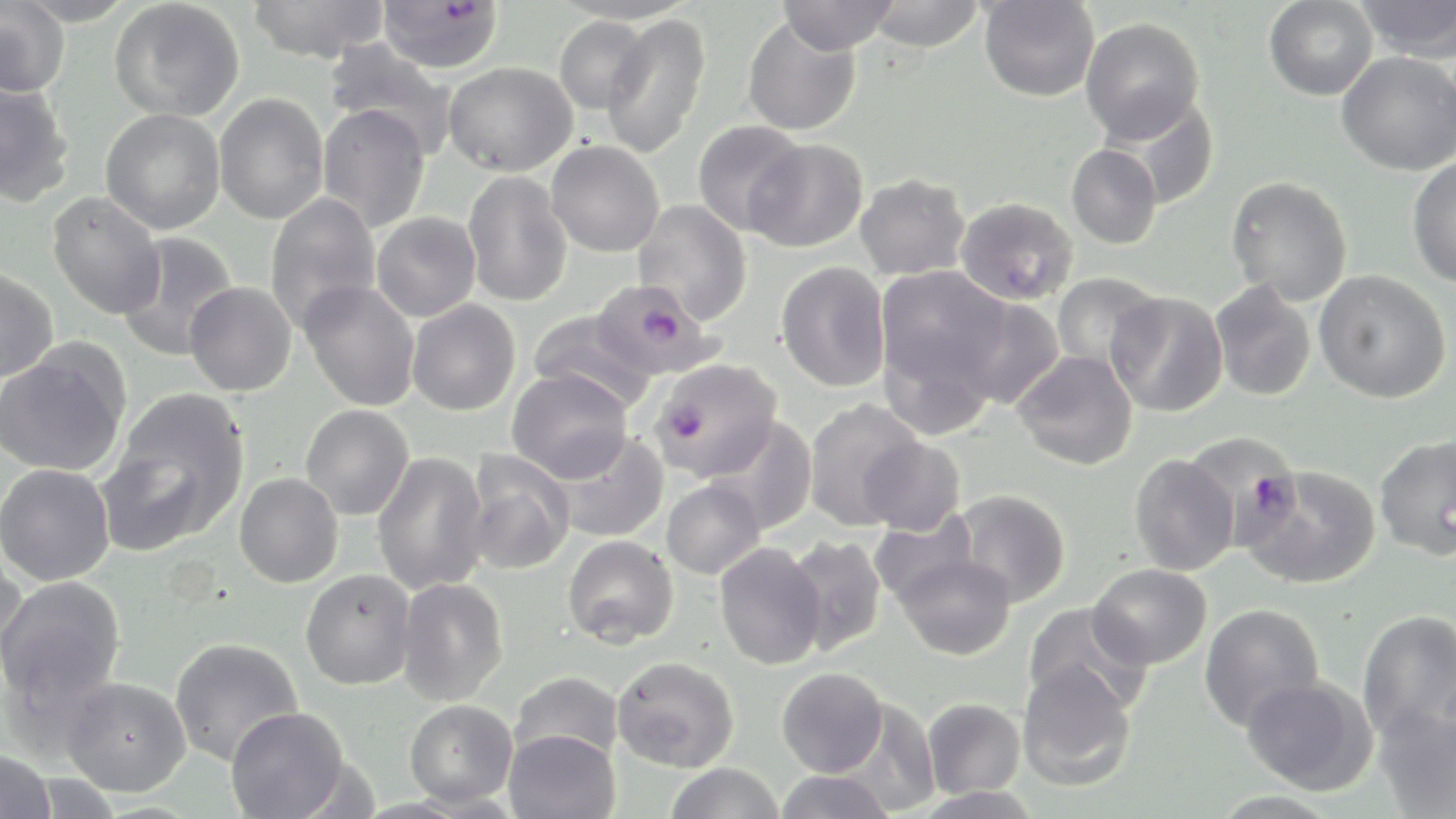

Approximate bounding boxes as named x1/y1/x2/y2 corners in pixels. Uninfected red blood cell locations: (x1=0, y1=0, x2=70, y2=99), (x1=18, y1=0, x2=134, y2=27), (x1=109, y1=0, x2=245, y2=123), (x1=775, y1=0, x2=901, y2=56), (x1=864, y1=0, x2=984, y2=53), (x1=978, y1=0, x2=1099, y2=102), (x1=1263, y1=0, x2=1378, y2=101), (x1=1355, y1=0, x2=1455, y2=61), (x1=246, y1=1, x2=391, y2=63), (x1=553, y1=1, x2=700, y2=25), (x1=601, y1=14, x2=711, y2=159), (x1=553, y1=15, x2=653, y2=114), (x1=742, y1=16, x2=862, y2=136), (x1=1080, y1=17, x2=1205, y2=144), (x1=323, y1=38, x2=458, y2=157), (x1=1336, y1=51, x2=1456, y2=175), (x1=443, y1=61, x2=578, y2=176), (x1=0, y1=78, x2=75, y2=207), (x1=213, y1=92, x2=329, y2=224), (x1=1110, y1=96, x2=1221, y2=210), (x1=316, y1=103, x2=431, y2=233), (x1=100, y1=108, x2=225, y2=234), (x1=692, y1=121, x2=808, y2=237), (x1=746, y1=139, x2=869, y2=253), (x1=546, y1=141, x2=664, y2=257), (x1=1066, y1=144, x2=1162, y2=249), (x1=1407, y1=156, x2=1456, y2=289), (x1=461, y1=171, x2=573, y2=307), (x1=856, y1=173, x2=971, y2=280), (x1=1225, y1=176, x2=1352, y2=306), (x1=47, y1=191, x2=165, y2=319), (x1=264, y1=192, x2=381, y2=331), (x1=955, y1=197, x2=1078, y2=306), (x1=632, y1=199, x2=753, y2=325), (x1=371, y1=211, x2=481, y2=321), (x1=115, y1=232, x2=239, y2=361), (x1=776, y1=261, x2=891, y2=393), (x1=875, y1=264, x2=1012, y2=419), (x1=0, y1=266, x2=59, y2=383), (x1=1313, y1=270, x2=1452, y2=403), (x1=1050, y1=271, x2=1165, y2=377), (x1=300, y1=280, x2=420, y2=412), (x1=184, y1=281, x2=297, y2=396), (x1=1209, y1=281, x2=1316, y2=401), (x1=1106, y1=291, x2=1229, y2=417), (x1=955, y1=295, x2=1065, y2=410), (x1=406, y1=299, x2=521, y2=415), (x1=528, y1=310, x2=656, y2=414), (x1=0, y1=343, x2=131, y2=477), (x1=1012, y1=350, x2=1139, y2=470), (x1=507, y1=369, x2=633, y2=482), (x1=99, y1=388, x2=250, y2=553), (x1=803, y1=398, x2=926, y2=530), (x1=300, y1=404, x2=414, y2=520), (x1=705, y1=415, x2=818, y2=535), (x1=551, y1=431, x2=669, y2=543), (x1=1374, y1=434, x2=1456, y2=560), (x1=858, y1=437, x2=966, y2=536), (x1=464, y1=450, x2=575, y2=575), (x1=371, y1=451, x2=490, y2=595), (x1=1129, y1=453, x2=1239, y2=576), (x1=0, y1=463, x2=115, y2=586), (x1=1241, y1=465, x2=1380, y2=589), (x1=234, y1=472, x2=344, y2=588), (x1=661, y1=478, x2=766, y2=579), (x1=952, y1=489, x2=1071, y2=607), (x1=869, y1=511, x2=981, y2=609), (x1=562, y1=535, x2=679, y2=647), (x1=781, y1=535, x2=887, y2=657), (x1=0, y1=542, x2=26, y2=671), (x1=714, y1=542, x2=826, y2=670), (x1=894, y1=553, x2=1017, y2=661), (x1=1088, y1=563, x2=1212, y2=669), (x1=300, y1=569, x2=417, y2=690), (x1=0, y1=575, x2=127, y2=712), (x1=396, y1=577, x2=509, y2=705), (x1=1022, y1=601, x2=1154, y2=718), (x1=1199, y1=603, x2=1325, y2=731), (x1=1357, y1=609, x2=1456, y2=741), (x1=169, y1=637, x2=303, y2=766), (x1=613, y1=655, x2=739, y2=772), (x1=1018, y1=661, x2=1137, y2=791), (x1=776, y1=667, x2=888, y2=777), (x1=510, y1=671, x2=623, y2=765), (x1=1242, y1=675, x2=1377, y2=795), (x1=59, y1=676, x2=191, y2=796), (x1=830, y1=695, x2=940, y2=816), (x1=923, y1=697, x2=1025, y2=799), (x1=404, y1=699, x2=517, y2=807), (x1=1372, y1=699, x2=1456, y2=818), (x1=225, y1=706, x2=351, y2=819), (x1=504, y1=728, x2=620, y2=819), (x1=0, y1=749, x2=56, y2=819), (x1=665, y1=762, x2=784, y2=819), (x1=774, y1=769, x2=895, y2=819). Plasmodium falciparum-infected red blood cell locations: (x1=377, y1=0, x2=504, y2=73), (x1=590, y1=278, x2=719, y2=380), (x1=650, y1=359, x2=781, y2=481), (x1=1182, y1=430, x2=1304, y2=551). Slide-level diagnosis: Plasmodium falciparum. Thin blood film. Image is 1456×819 pixels. Single field of view. Light microscopy. May-Grünwald-Giemsa-stained preparation. Captured at 1000x magnification.